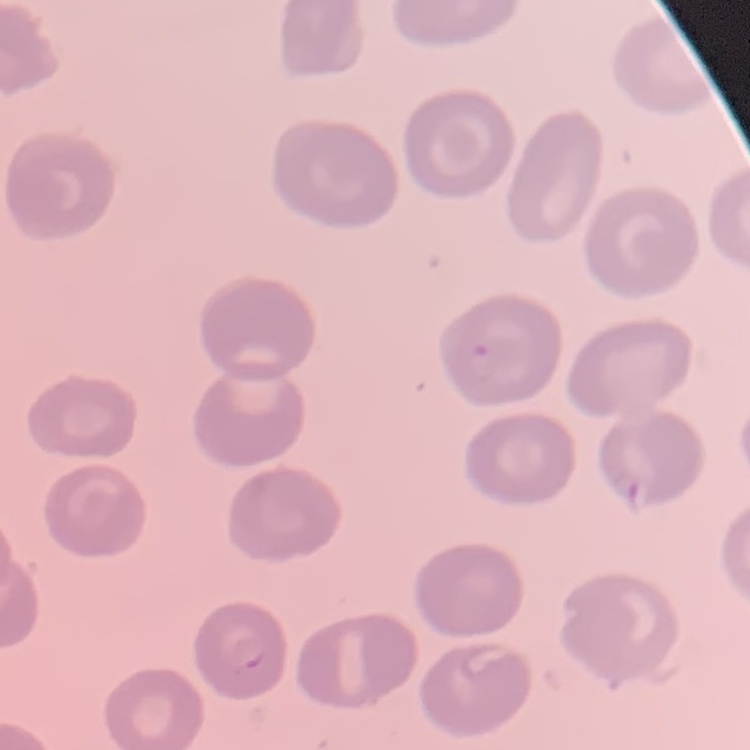

erythrocyte morphology = no rouleaux formation
image type = one tile cut from a larger photomicrograph
preparation = thin blood film
stain = Field's or Giemsa